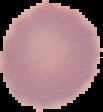

image size = 103×112 pixels
image type = segmented cell region on a black background
preparation = thin blood smear
result = no Plasmodium parasites detected